Classify this cell by malaria status.
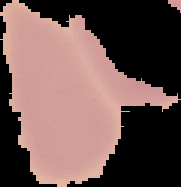

It is uninfected.

image size = 181×187 pixels
image type = segmented cell region with the area outside set to black
preparation = thin blood film